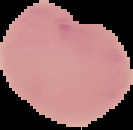

Summary:
  - Result: negative for Plasmodium parasites
  - Preparation: thin blood film
  - Image type: segmented cell region on a black background
  - Image size: 133×130 pixels